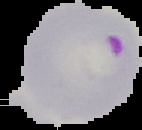
Summary:
  - Preparation: thin blood film
  - Image type: segmented cell region with the area outside set to black
  - Image size: 142×130 pixels
  - Result: Plasmodium parasites identified